Describe the morphology of the red blood cells.
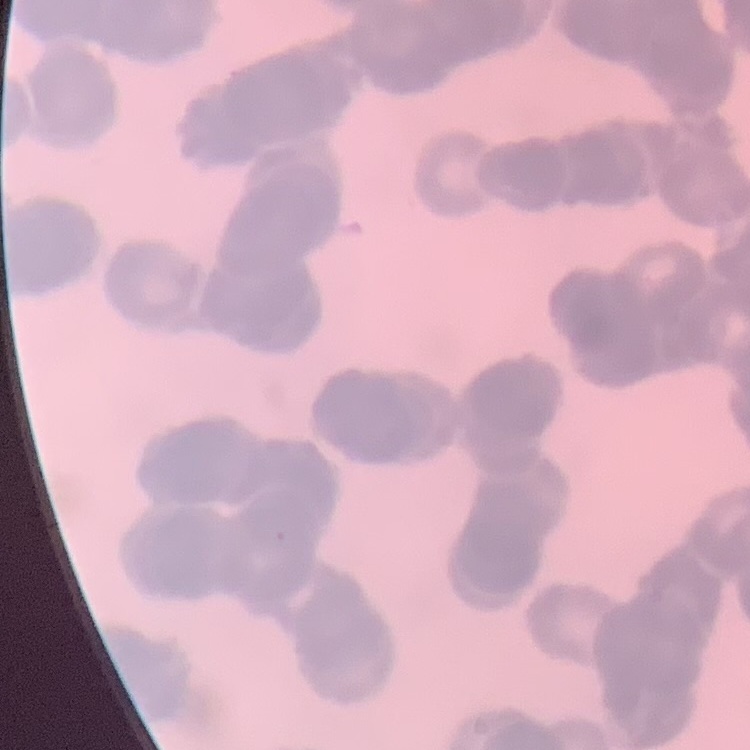
Rouleaux formation.

{
  "image_type": "one tile cut from a larger photomicrograph",
  "preparation": "thin peripheral smear",
  "stain": "Field's or Giemsa"
}